Point out cells.
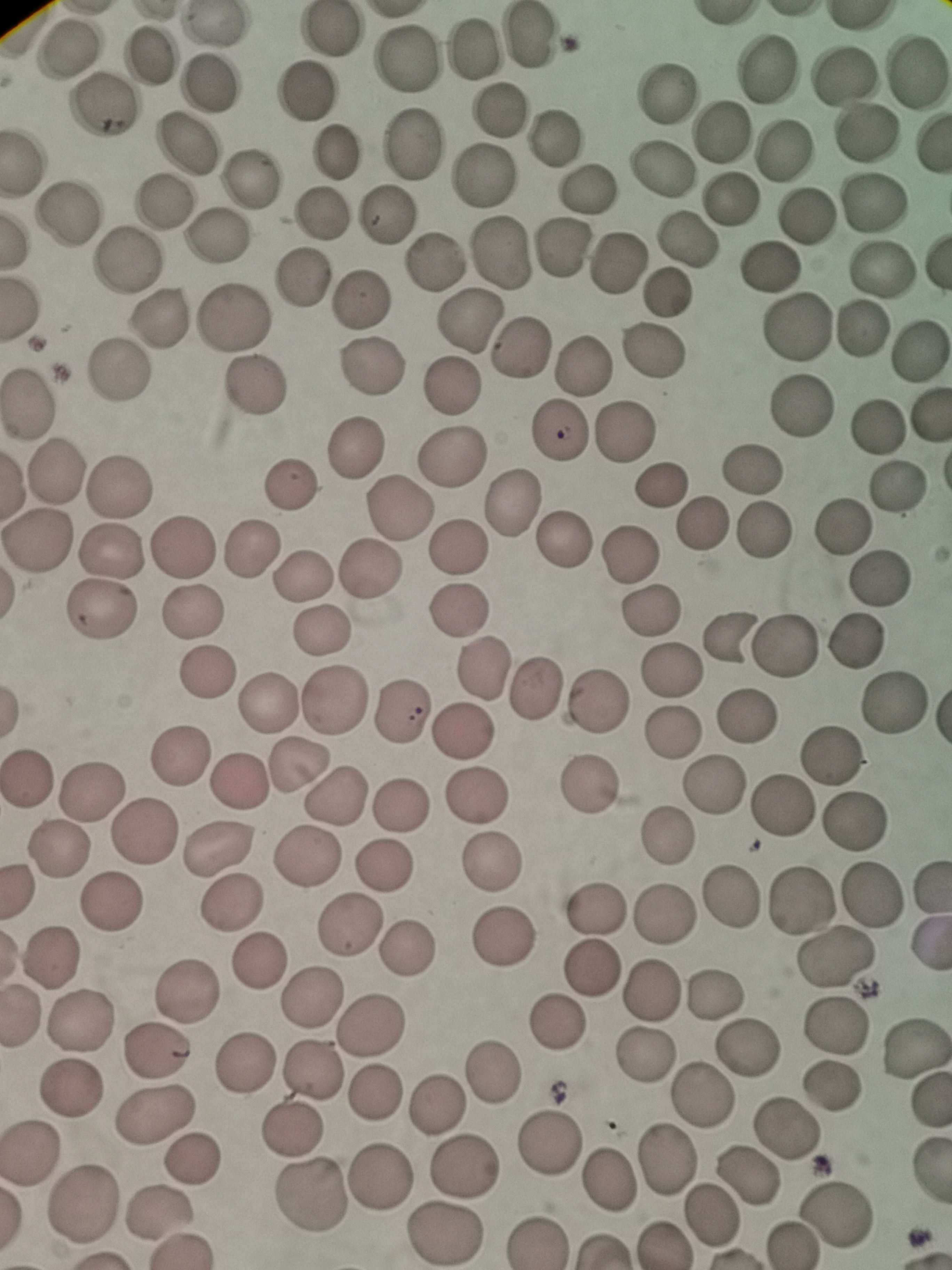

Approximate centers as [x, y] in pixels.
Cells: [212, 25], [329, 30], [530, 39], [475, 47], [68, 50], [153, 56], [407, 60], [769, 68], [917, 73], [842, 75], [210, 82], [307, 91], [663, 94], [105, 105], [499, 109], [718, 131], [866, 133], [552, 137], [413, 142], [188, 143], [781, 151], [335, 152], [659, 172], [482, 176], [249, 178], [583, 190], [728, 200], [873, 201], [165, 203], [71, 212], [386, 213], [323, 215], [808, 219], [215, 236], [683, 242], [564, 247], [504, 254], [618, 259], [128, 260], [434, 263], [881, 265], [767, 266], [301, 280], [666, 291], [362, 298], [235, 313], [161, 316], [471, 319], [795, 326], [864, 328], [521, 347], [919, 349], [651, 353], [585, 365], [367, 371], [120, 373], [254, 384], [453, 387], [31, 403], [800, 406], [877, 430], [555, 431], [627, 432], [354, 448], [450, 456], [54, 470], [751, 471], [118, 484], [290, 486], [660, 486], [898, 486], [514, 497], [397, 508], [705, 524], [843, 524], [768, 530], [566, 535], [37, 536], [186, 544], [455, 545], [251, 546], [111, 551], [629, 553], [367, 569], [302, 577], [881, 579], [461, 608], [654, 610], [101, 611], [192, 612], [322, 630], [730, 632], [856, 637], [788, 643], [485, 667], [670, 667], [204, 674], [534, 687], [596, 698], [337, 699], [896, 701], [268, 704], [401, 713], [746, 716], [671, 731], [462, 733], [182, 755], [830, 757], [299, 765], [30, 777], [238, 779], [590, 784], [715, 787], [91, 788], [334, 796], [482, 797], [400, 802], [781, 805], [855, 822], [146, 833], [668, 836], [218, 849], [58, 852], [310, 855], [491, 862], [388, 863], [802, 898], [874, 898], [732, 899], [112, 901], [232, 901], [595, 911], [664, 915], [349, 925], [502, 937], [406, 946], [51, 957], [835, 959], [262, 961], [593, 969], [187, 989], [650, 991], [716, 991], [313, 998], [80, 1019], [835, 1024], [375, 1025], [557, 1026], [915, 1048], [747, 1049], [160, 1052], [646, 1056], [248, 1062], [311, 1068], [493, 1071], [833, 1084], [73, 1087], [376, 1093], [703, 1094], [439, 1104], [153, 1115], [788, 1129], [291, 1131], [548, 1139], [29, 1151], [193, 1159], [662, 1161], [469, 1165], [746, 1173], [381, 1179], [609, 1182], [310, 1197], [85, 1205], [160, 1212], [711, 1213], [838, 1213], [445, 1235], [536, 1242], [793, 1244], [663, 1245].

Summary:
  - Capture: smartphone camera at the microscope eyepiece
  - Stain: Giemsa
  - Preparation: thin blood smear
  - Field of view: single
  - Image size: 952×1270 pixels